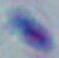

{
  "modality": "photomicrograph",
  "identification": "Toxoplasma gondii",
  "magnification": "1000x"
}